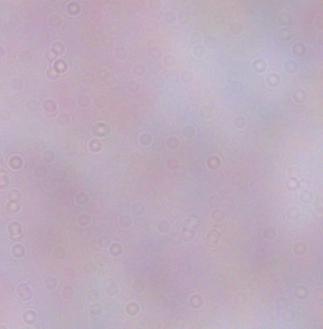

Summary:
  - Modality: photomicrograph
  - Identification: trypanosome
  - Magnification: 1000x